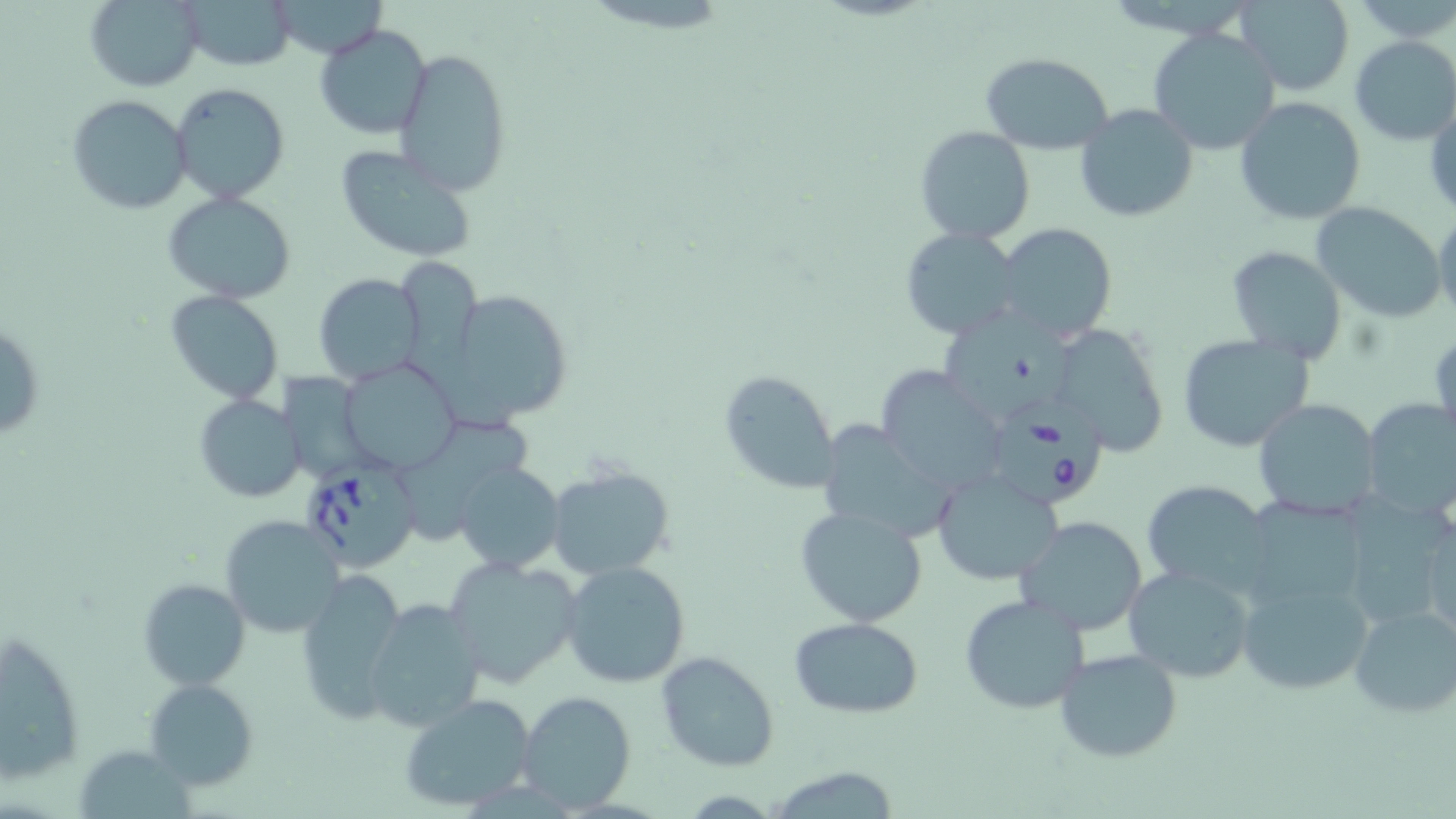
Approximate bounding boxes as named x1/y1/x2/y2 corners in pixels. Uninfected red blood cell locations: (x1=84, y1=0, x2=204, y2=92), (x1=180, y1=0, x2=297, y2=69), (x1=1235, y1=1, x2=1355, y2=94), (x1=273, y1=2, x2=389, y2=58), (x1=314, y1=24, x2=434, y2=141), (x1=1148, y1=26, x2=1279, y2=158), (x1=1349, y1=36, x2=1456, y2=147), (x1=394, y1=48, x2=511, y2=196), (x1=979, y1=51, x2=1113, y2=156), (x1=172, y1=82, x2=291, y2=204), (x1=66, y1=94, x2=191, y2=214), (x1=1234, y1=96, x2=1367, y2=226), (x1=1426, y1=97, x2=1456, y2=225), (x1=1074, y1=103, x2=1199, y2=223), (x1=914, y1=125, x2=1035, y2=244), (x1=334, y1=144, x2=480, y2=265), (x1=161, y1=191, x2=298, y2=305), (x1=1309, y1=200, x2=1447, y2=322), (x1=1433, y1=209, x2=1456, y2=319), (x1=994, y1=222, x2=1117, y2=343), (x1=900, y1=227, x2=1024, y2=341), (x1=1226, y1=245, x2=1348, y2=363), (x1=399, y1=259, x2=483, y2=393), (x1=314, y1=272, x2=425, y2=384), (x1=442, y1=286, x2=573, y2=420), (x1=166, y1=291, x2=283, y2=405), (x1=946, y1=307, x2=1073, y2=415), (x1=1, y1=317, x2=47, y2=449), (x1=1047, y1=325, x2=1169, y2=456), (x1=1174, y1=333, x2=1318, y2=455), (x1=339, y1=359, x2=461, y2=474), (x1=875, y1=367, x2=1006, y2=493), (x1=720, y1=369, x2=841, y2=494), (x1=275, y1=371, x2=383, y2=481), (x1=195, y1=394, x2=305, y2=504), (x1=1251, y1=398, x2=1384, y2=520), (x1=1360, y1=398, x2=1454, y2=521), (x1=407, y1=416, x2=534, y2=542), (x1=821, y1=418, x2=954, y2=538), (x1=454, y1=461, x2=566, y2=572), (x1=546, y1=463, x2=676, y2=581), (x1=931, y1=468, x2=1064, y2=587), (x1=1142, y1=480, x2=1277, y2=592), (x1=1334, y1=495, x2=1454, y2=637), (x1=1419, y1=502, x2=1456, y2=642), (x1=794, y1=504, x2=927, y2=627), (x1=221, y1=515, x2=346, y2=640), (x1=1015, y1=515, x2=1150, y2=637), (x1=441, y1=554, x2=586, y2=689), (x1=561, y1=560, x2=691, y2=687), (x1=1122, y1=563, x2=1256, y2=684), (x1=295, y1=572, x2=410, y2=725), (x1=1237, y1=573, x2=1372, y2=696), (x1=139, y1=577, x2=249, y2=690), (x1=959, y1=593, x2=1091, y2=714), (x1=363, y1=597, x2=486, y2=732), (x1=1348, y1=603, x2=1456, y2=719), (x1=789, y1=616, x2=923, y2=718), (x1=1, y1=630, x2=85, y2=784), (x1=1053, y1=649, x2=1183, y2=764), (x1=656, y1=651, x2=780, y2=771), (x1=145, y1=678, x2=261, y2=790), (x1=516, y1=690, x2=636, y2=812), (x1=398, y1=692, x2=537, y2=812), (x1=80, y1=745, x2=200, y2=819), (x1=766, y1=766, x2=903, y2=818). Babesia divergens-infected red blood cell locations: (x1=996, y1=393, x2=1107, y2=509), (x1=296, y1=461, x2=424, y2=573). Slide-level diagnosis: Babesia divergens. May-Grünwald-Giemsa stain. Single field of view. Optical microscopy. Image is 1456×819 pixels. Thin blood film. 1000x magnification.